Assess this cell for malaria.
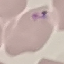
It is parasitized.

{
  "stain": "Giemsa",
  "image_type": "cell patch, automatically extracted from a larger field of view and resized to 64 × 64 pixels",
  "capture": "smartphone camera at the microscope eyepiece",
  "preparation": "thin blood film"
}